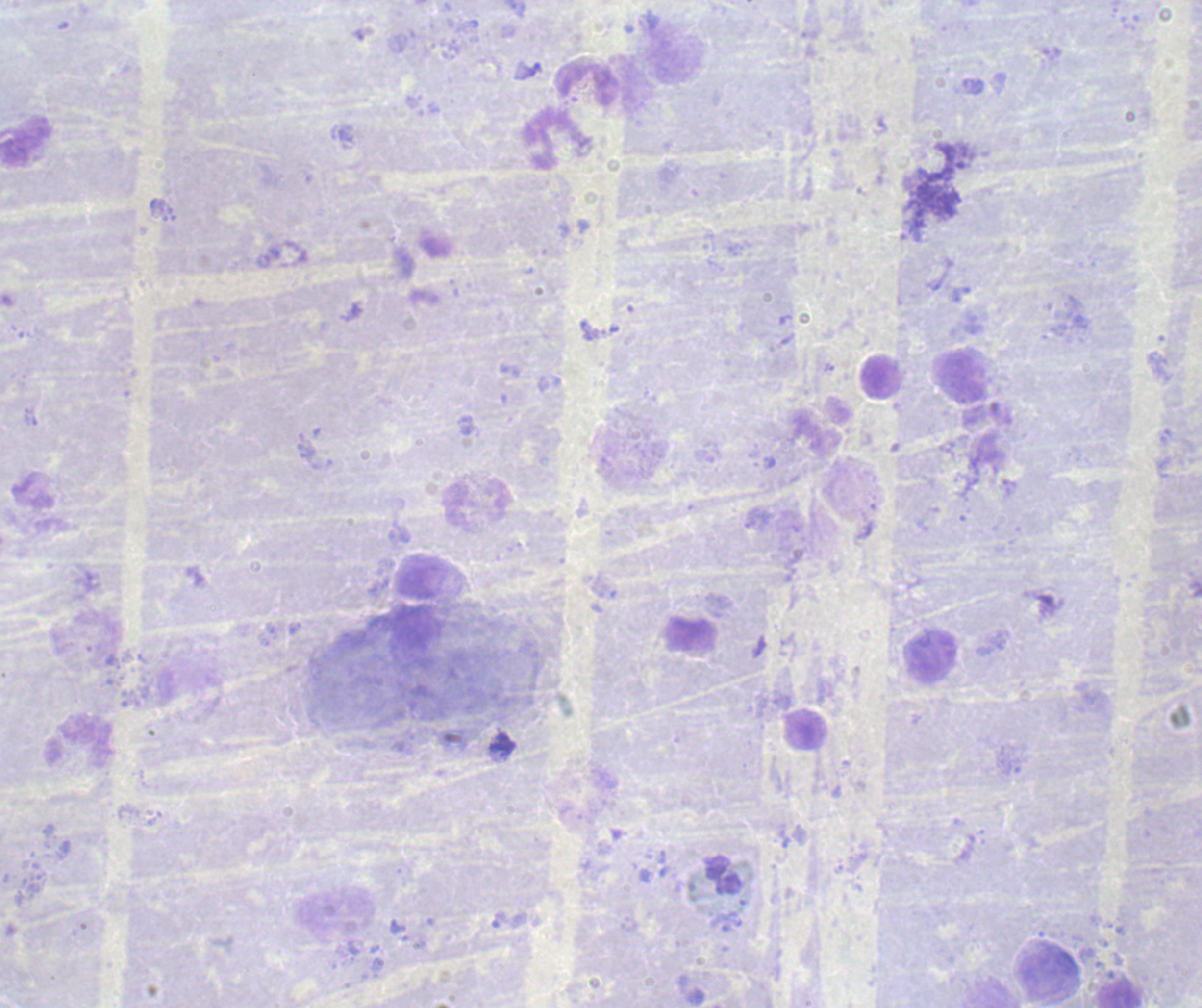
Approximate centers as (x, y) in pixels.
Summary:
  - Leukocyte locations: (589, 82), (960, 377), (881, 378), (932, 658), (79, 740)
  - Result: no malaria parasites seen
  - Context: previously used in a real diagnosis
  - Image size: 1202×1008 pixels
  - Background quality: unsatisfactory
  - Preparation: thick smear of blood
  - Field of view: one from this slide
  - Magnification: 100x
  - Stain: Romanowsky